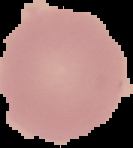
Image is 133×148 pixels. The area outside the segmented cell region is set to black. From a thin blood film. Result: negative for malaria parasites.